Assess this cell for malaria.
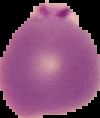

It is parasitized.

{
  "preparation": "thin blood smear",
  "image_type": "segmented cell region on a black background",
  "image_size": "100×118 pixels"
}